Look for parasitized red blood cells.
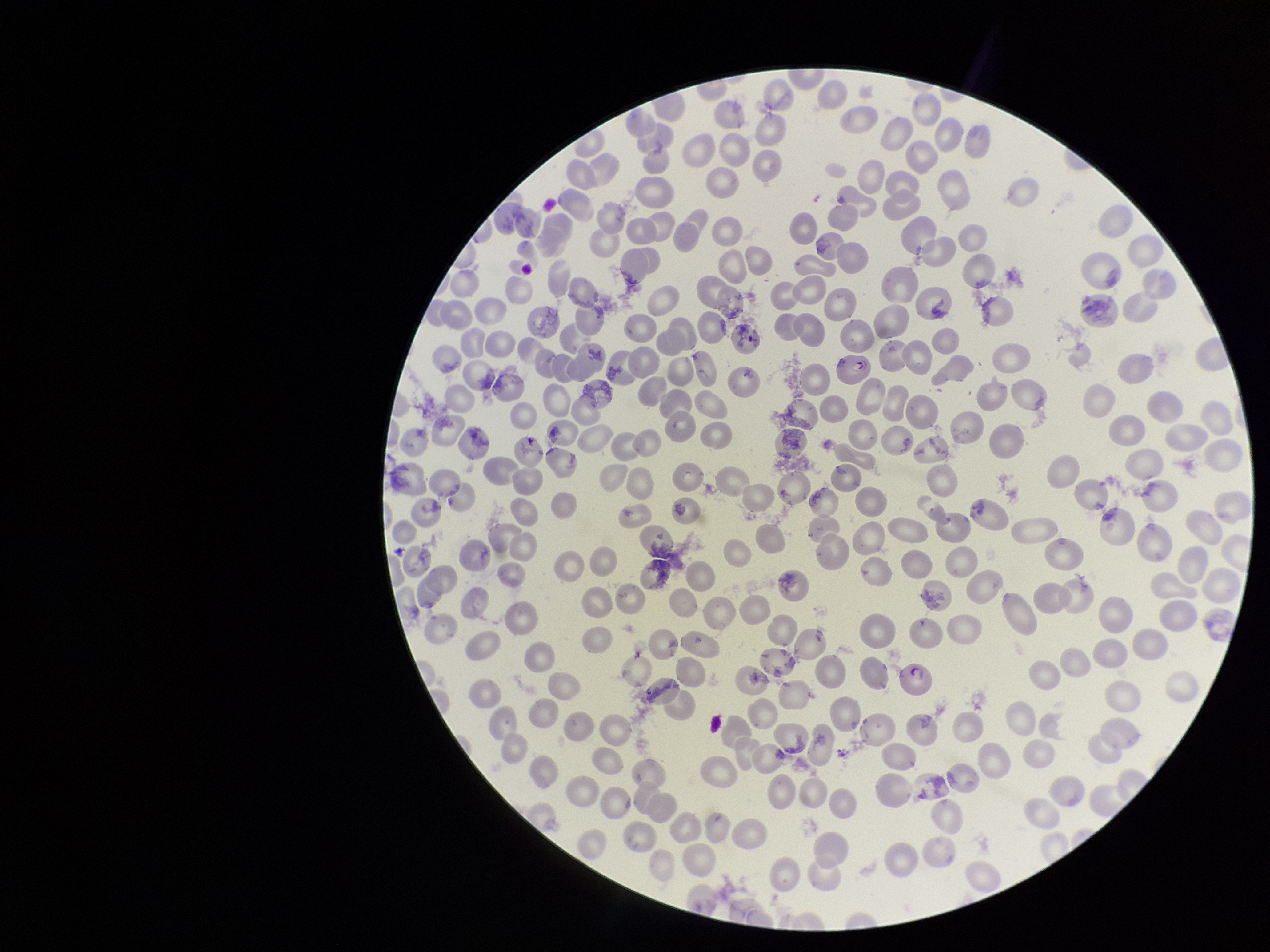
Detected.

Species reported for this patient: Plasmodium falciparum. Preparation: thin. Red blood cell count: 225. Image is 1270×952 pixels. Parasitized red blood cell count: 1. Stained with Giemsa. Single field of view. Patient malaria status: positive. Photographed through the microscope eyepiece with a smartphone camera.